Assess this cell for malaria.
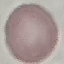
It is uninfected.

{
  "preparation": "thin blood smear",
  "capture": "smartphone camera at the microscope eyepiece",
  "image_type": "cell patch, automatically extracted from a larger field of view and resized to 64 × 64 pixels",
  "stain": "Giemsa"
}